Locate every blood parasite and identify its species.
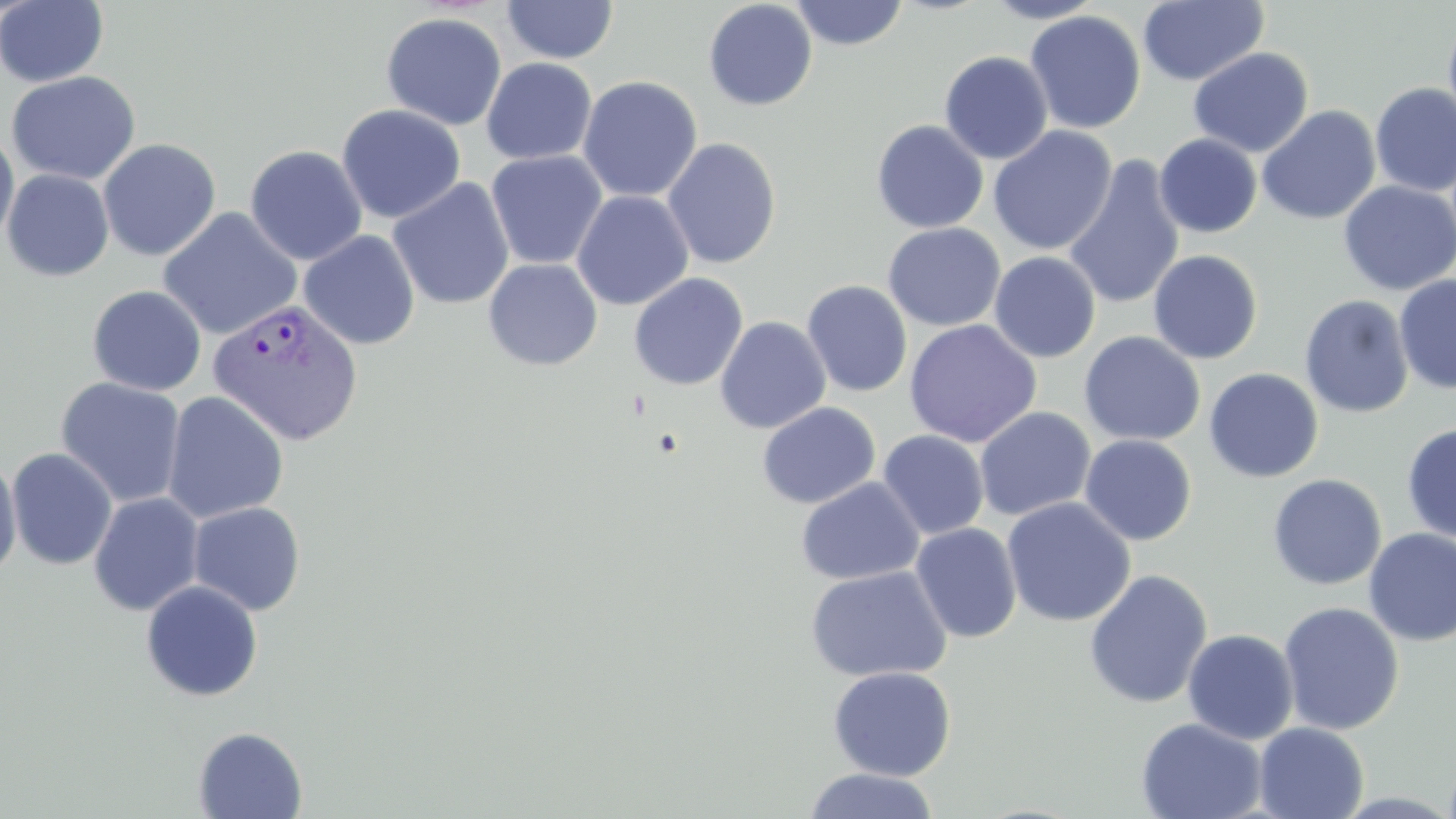

Approximate bounding boxes as named x1/y1/x2/y2 corners in pixels.
Plasmodium vivax-infected red blood cells: (x1=207, y1=297, x2=364, y2=446).
No Plasmodium falciparum, Plasmodium ovale, Plasmodium malariae, Babesia divergens, or Trypanosoma brucei observed.

Uninfected red blood cell locations: (x1=0, y1=0, x2=110, y2=88), (x1=984, y1=0, x2=1105, y2=23), (x1=1138, y1=0, x2=1269, y2=86), (x1=502, y1=1, x2=618, y2=65), (x1=702, y1=1, x2=818, y2=111), (x1=789, y1=1, x2=910, y2=51), (x1=1025, y1=10, x2=1146, y2=134), (x1=1443, y1=10, x2=1456, y2=136), (x1=380, y1=12, x2=507, y2=131), (x1=1188, y1=47, x2=1314, y2=157), (x1=939, y1=51, x2=1053, y2=164), (x1=481, y1=58, x2=597, y2=165), (x1=5, y1=71, x2=141, y2=185), (x1=577, y1=76, x2=702, y2=202), (x1=1370, y1=82, x2=1456, y2=197), (x1=336, y1=104, x2=466, y2=224), (x1=1257, y1=105, x2=1381, y2=226), (x1=871, y1=119, x2=989, y2=233), (x1=988, y1=126, x2=1117, y2=256), (x1=0, y1=127, x2=20, y2=252), (x1=1154, y1=133, x2=1262, y2=238), (x1=98, y1=138, x2=221, y2=261), (x1=662, y1=138, x2=782, y2=269), (x1=245, y1=145, x2=367, y2=265), (x1=486, y1=150, x2=608, y2=270), (x1=1063, y1=155, x2=1185, y2=311), (x1=2, y1=169, x2=114, y2=282), (x1=387, y1=178, x2=514, y2=310), (x1=1338, y1=181, x2=1456, y2=295), (x1=572, y1=189, x2=694, y2=311), (x1=157, y1=207, x2=302, y2=341), (x1=882, y1=222, x2=1006, y2=332), (x1=298, y1=230, x2=420, y2=350), (x1=1148, y1=249, x2=1263, y2=364), (x1=988, y1=251, x2=1100, y2=363), (x1=483, y1=258, x2=603, y2=371), (x1=628, y1=273, x2=748, y2=390), (x1=1394, y1=274, x2=1456, y2=395), (x1=802, y1=280, x2=913, y2=397), (x1=87, y1=285, x2=207, y2=396), (x1=1299, y1=295, x2=1414, y2=419), (x1=715, y1=316, x2=831, y2=434), (x1=904, y1=319, x2=1042, y2=448), (x1=1078, y1=331, x2=1206, y2=446), (x1=1203, y1=368, x2=1323, y2=483), (x1=55, y1=377, x2=187, y2=508), (x1=162, y1=391, x2=289, y2=524), (x1=757, y1=402, x2=880, y2=509), (x1=974, y1=407, x2=1096, y2=521), (x1=1401, y1=423, x2=1456, y2=543), (x1=877, y1=430, x2=989, y2=541), (x1=1079, y1=435, x2=1197, y2=546), (x1=5, y1=448, x2=118, y2=571), (x1=0, y1=454, x2=22, y2=583), (x1=1267, y1=473, x2=1387, y2=591), (x1=795, y1=477, x2=925, y2=585), (x1=88, y1=492, x2=205, y2=616), (x1=1001, y1=497, x2=1137, y2=627), (x1=188, y1=501, x2=306, y2=616), (x1=910, y1=523, x2=1022, y2=643), (x1=1363, y1=529, x2=1456, y2=646), (x1=804, y1=565, x2=952, y2=683), (x1=1083, y1=569, x2=1213, y2=709), (x1=140, y1=580, x2=264, y2=702), (x1=1278, y1=601, x2=1405, y2=735), (x1=1182, y1=628, x2=1300, y2=745), (x1=828, y1=666, x2=956, y2=781), (x1=1135, y1=717, x2=1267, y2=819), (x1=1254, y1=722, x2=1369, y2=819), (x1=193, y1=726, x2=307, y2=818), (x1=802, y1=768, x2=941, y2=819). Slide-level diagnosis: Plasmodium vivax. May-Grünwald-Giemsa-stained preparation. Image is 1456×819 pixels. Thin blood smear. Single field of view. Light microscopy. 1000x magnification.